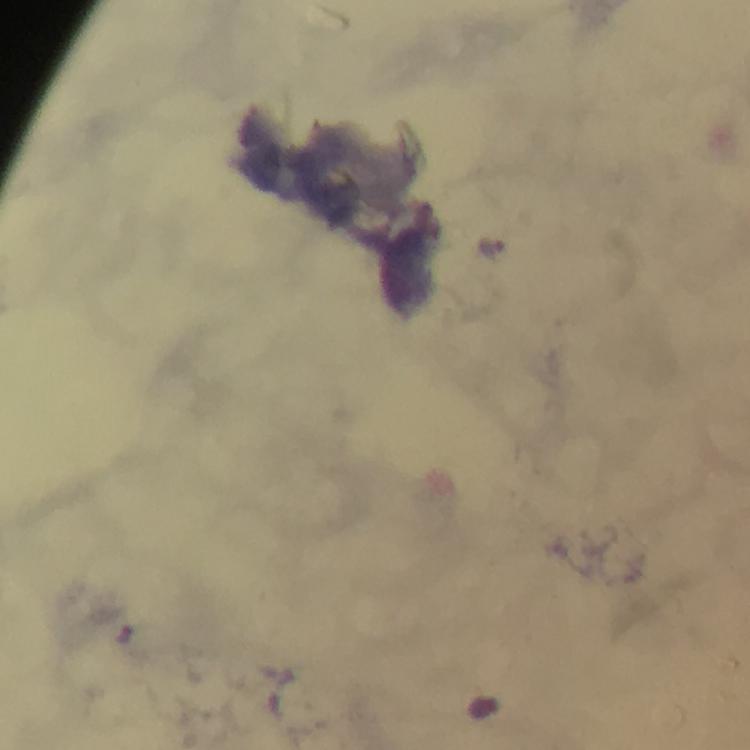
{
  "context": "from a malaria diagnostic workup",
  "stain": "Giemsa",
  "preparation": "thick blood smear",
  "image_size": "750×750 pixels",
  "immersion_oil": "applied",
  "magnification": "100x",
  "plasmodium_parasite_locations": "approximate centers as (x, y) in pixels: (491, 248)",
  "cropped_from": "a single field of view",
  "capture": "smartphone mounted on the microscope"
}